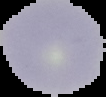

Result: negative for Plasmodium parasites. The area outside the segmented cell region is set to black. From a thin blood smear. Image is 106×97 pixels.